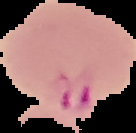
Malaria status: parasitized. From a thin blood film. The area outside the segmented cell region is set to black. Image is 136×133 pixels.